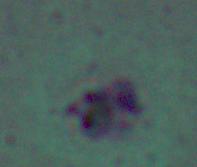
magnification = 1000x
modality = photomicrograph
identification = Leishmania